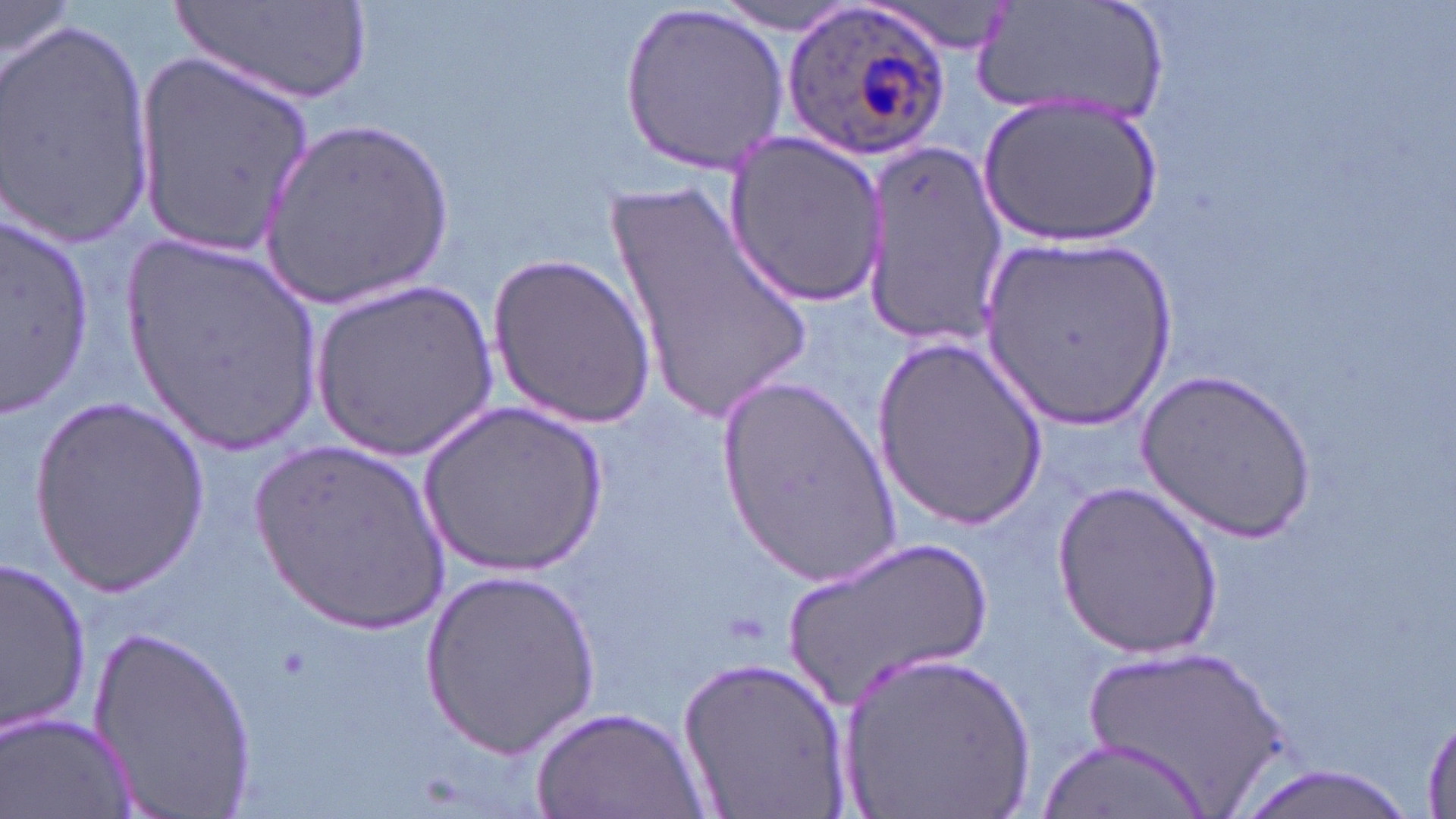

Summary:
  - Coordinate format: approximate bounding boxes as named x1/y1/x2/y2 corners in pixels
  - Uninfected red blood cell locations: (x1=0, y1=0, x2=76, y2=68), (x1=175, y1=0, x2=378, y2=110), (x1=868, y1=0, x2=1024, y2=56), (x1=974, y1=1, x2=1169, y2=126), (x1=711, y1=2, x2=864, y2=36), (x1=619, y1=3, x2=790, y2=172), (x1=0, y1=18, x2=155, y2=245), (x1=134, y1=49, x2=319, y2=256), (x1=981, y1=97, x2=1164, y2=247), (x1=262, y1=116, x2=454, y2=312), (x1=723, y1=128, x2=886, y2=304), (x1=864, y1=138, x2=1007, y2=347), (x1=601, y1=180, x2=819, y2=428), (x1=0, y1=219, x2=100, y2=410), (x1=123, y1=235, x2=326, y2=456), (x1=982, y1=238, x2=1173, y2=427), (x1=487, y1=251, x2=657, y2=430), (x1=312, y1=279, x2=500, y2=461), (x1=872, y1=335, x2=1048, y2=528), (x1=1138, y1=370, x2=1317, y2=541), (x1=716, y1=371, x2=902, y2=581), (x1=29, y1=395, x2=210, y2=598), (x1=418, y1=401, x2=610, y2=574), (x1=250, y1=439, x2=452, y2=634), (x1=1051, y1=481, x2=1227, y2=659), (x1=780, y1=530, x2=995, y2=713), (x1=2, y1=557, x2=93, y2=737), (x1=418, y1=566, x2=600, y2=760), (x1=90, y1=622, x2=260, y2=817), (x1=1074, y1=641, x2=1292, y2=810), (x1=836, y1=647, x2=1037, y2=817), (x1=676, y1=654, x2=854, y2=819), (x1=531, y1=704, x2=707, y2=819), (x1=1423, y1=711, x2=1456, y2=816), (x1=5, y1=713, x2=135, y2=818), (x1=1037, y1=736, x2=1215, y2=819), (x1=1227, y1=764, x2=1428, y2=819)
  - Plasmodium ovale-infected red blood cell locations: (x1=783, y1=2, x2=951, y2=163)
  - Slide-level diagnosis: Plasmodium ovale
  - Preparation: thin blood smear
  - Modality: optical microscopy
  - Magnification: 1000x
  - Image size: 1456×819 pixels
  - Stain: May-Grünwald-Giemsa
  - Field of view: one of a larger specimen